Describe the morphology of the red blood cells.
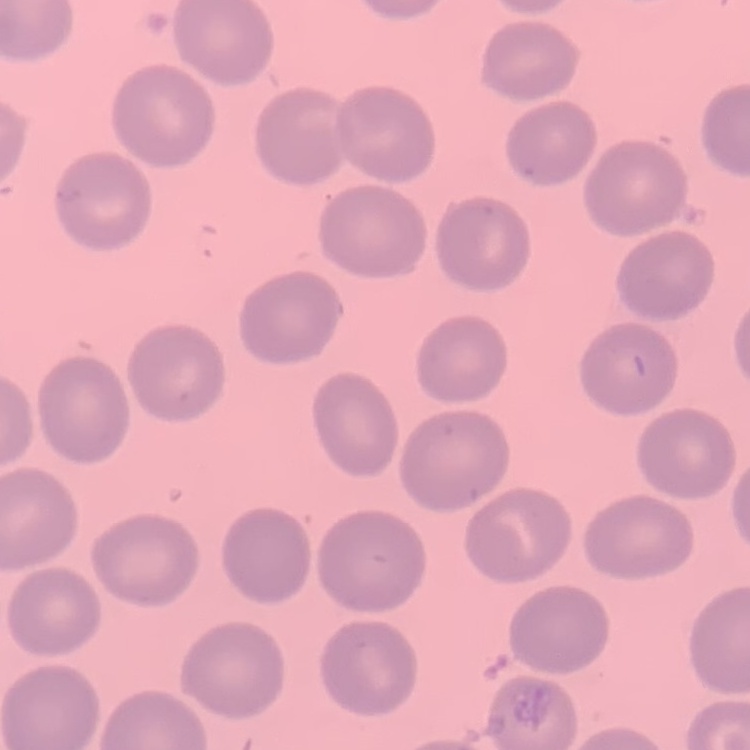
No rouleaux formation.

stain: Field's or Giemsa
image_type: square crop of a larger photomicrograph
preparation: thin blood smear